Name the blood parasite species.
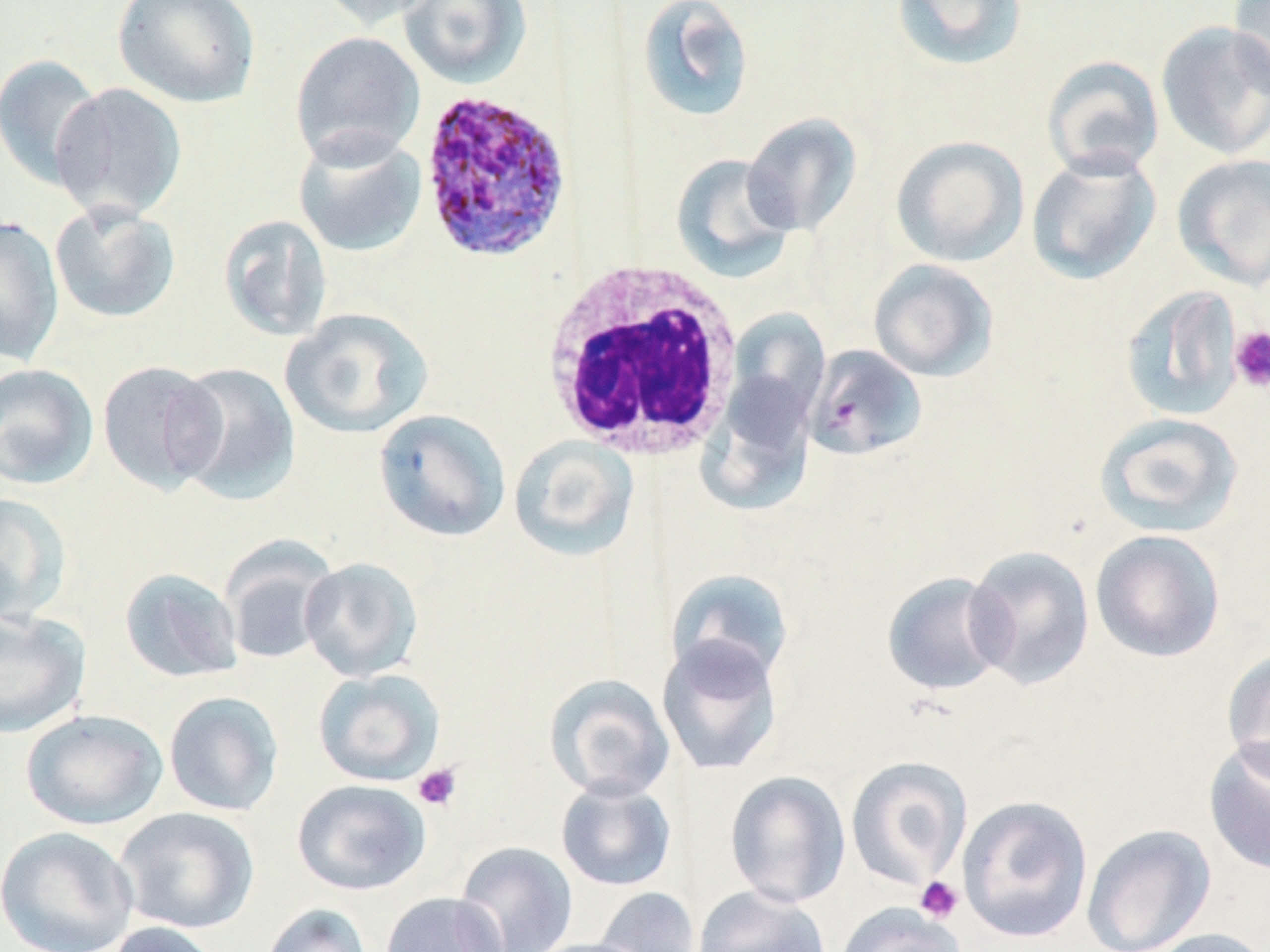
Plasmodium ovale.

uninfected red blood cell locations = approximate bounding boxes as [x1, y1, x2, y2] in pixels: [112, 0, 261, 108], [317, 0, 441, 30], [398, 0, 532, 89], [890, 0, 1029, 72], [1227, 0, 1270, 99], [635, 1, 755, 123], [1156, 20, 1270, 161], [290, 30, 425, 168], [0, 54, 106, 190], [1041, 55, 1165, 181], [51, 83, 188, 223], [741, 113, 862, 236], [292, 129, 427, 258], [890, 135, 1029, 268], [1025, 149, 1162, 286], [1171, 153, 1270, 291], [670, 154, 798, 282], [49, 200, 182, 324], [218, 214, 333, 341], [0, 216, 64, 366], [868, 258, 998, 382], [1119, 285, 1244, 422], [280, 307, 432, 439], [726, 308, 830, 427], [804, 345, 926, 461], [97, 360, 226, 494], [168, 361, 301, 505], [0, 362, 99, 490], [697, 371, 819, 516], [373, 408, 512, 542], [1094, 412, 1244, 537], [509, 435, 640, 561], [0, 493, 72, 625], [1090, 529, 1226, 663], [221, 540, 337, 666], [963, 545, 1095, 691], [299, 557, 424, 682], [119, 568, 243, 683], [665, 568, 796, 687], [881, 571, 1012, 697], [0, 608, 91, 738], [655, 635, 784, 776], [1222, 648, 1270, 782], [313, 668, 445, 786], [544, 674, 675, 801], [163, 690, 284, 816], [20, 709, 168, 830], [1203, 736, 1270, 876], [845, 755, 973, 889], [724, 770, 851, 908], [555, 778, 677, 892], [291, 779, 431, 896], [957, 794, 1093, 943], [114, 806, 260, 935], [1081, 823, 1216, 952], [0, 826, 140, 952], [454, 841, 578, 952], [692, 885, 833, 952], [593, 886, 701, 952], [381, 892, 507, 952], [260, 902, 372, 952], [835, 903, 967, 952], [103, 921, 225, 952], [1138, 927, 1270, 952], [525, 938, 654, 952]
Plasmodium ovale-infected red blood cell locations = approximate bounding boxes as [x1, y1, x2, y2] in pixels: [416, 89, 574, 264]
white blood cell locations = approximate bounding boxes as [x1, y1, x2, y2] in pixels: [541, 261, 744, 461]
image size = 1270×952 pixels
preparation = thin blood film
stain = May-Grünwald-Giemsa
platelet locations = approximate bounding boxes as [x1, y1, x2, y2] in pixels: [1229, 326, 1270, 392], [412, 763, 462, 812], [914, 876, 965, 923]
magnification = 1000x
field of view = one of a larger specimen
modality = optical microscopy